Assess this cell for malaria.
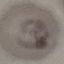

It is parasitized.

{
  "image_type": "automatically extracted cell patch, resized to 64 × 64 pixels",
  "stain": "Giemsa",
  "capture": "smartphone camera at the microscope eyepiece",
  "preparation": "thin blood smear"
}